Identify the parasite.
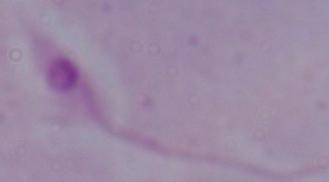

This is Leishmania.

Summary:
  - Magnification: 1000x
  - Modality: photomicrograph